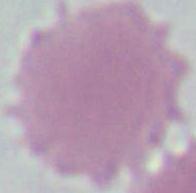
magnification = 1000x
identification = red blood cell
modality = photomicrograph